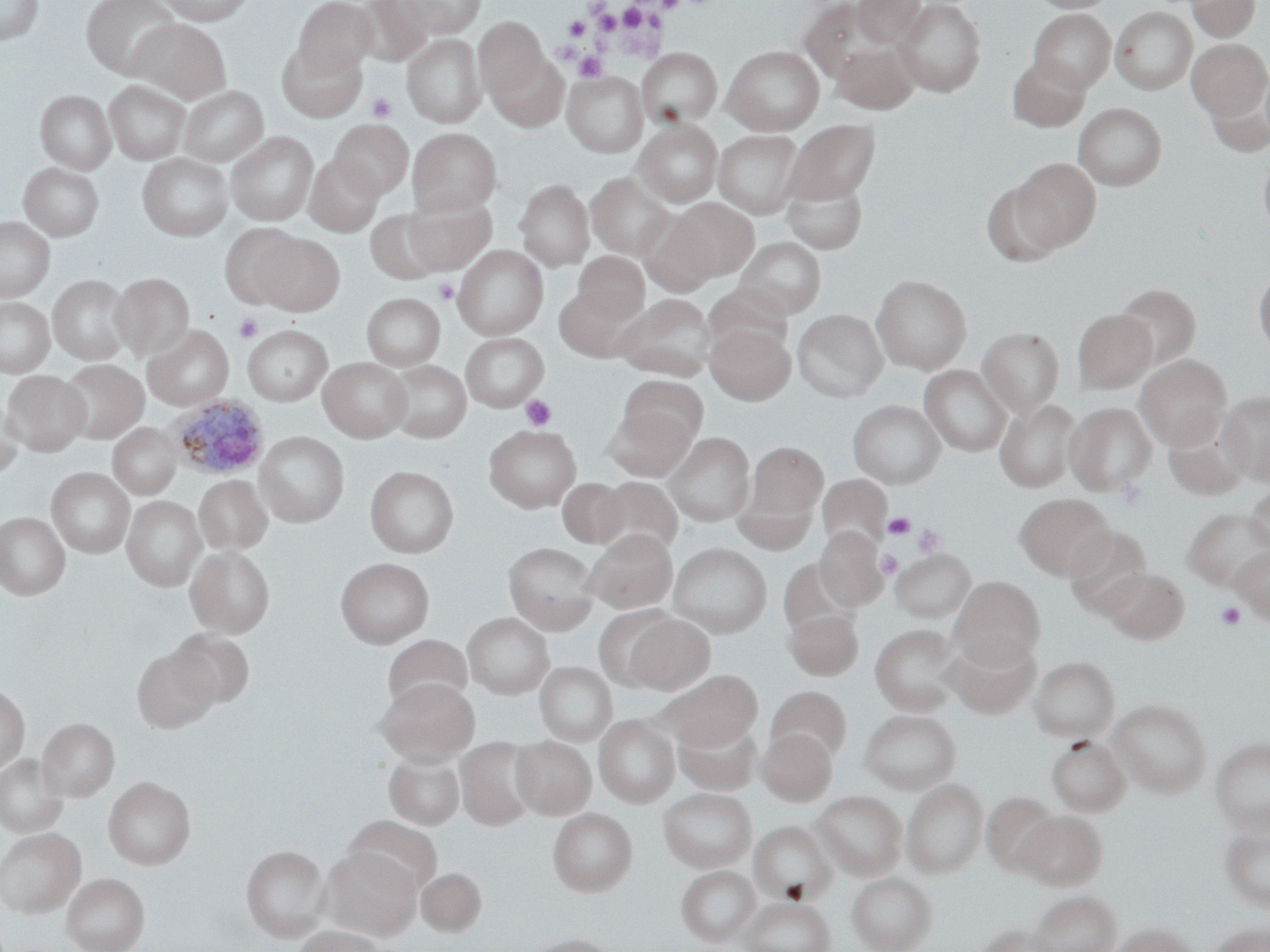
Summary:
  - Coordinate format: approximate bounding boxes as named x1/y1/x2/y2 corners in pixels
  - Platelet locations: (x1=618, y1=3, x2=650, y2=30), (x1=590, y1=5, x2=621, y2=33), (x1=565, y1=16, x2=590, y2=39), (x1=573, y1=51, x2=607, y2=82), (x1=367, y1=93, x2=397, y2=122), (x1=433, y1=278, x2=460, y2=304), (x1=234, y1=315, x2=262, y2=342), (x1=520, y1=394, x2=556, y2=430), (x1=883, y1=512, x2=915, y2=539), (x1=912, y1=523, x2=945, y2=557), (x1=876, y1=551, x2=903, y2=579), (x1=1215, y1=602, x2=1246, y2=631)
  - Uninfected red blood cell locations: (x1=0, y1=0, x2=43, y2=44), (x1=82, y1=0, x2=181, y2=79), (x1=160, y1=0, x2=253, y2=25), (x1=293, y1=0, x2=378, y2=76), (x1=354, y1=0, x2=433, y2=67), (x1=399, y1=0, x2=485, y2=37), (x1=852, y1=0, x2=928, y2=47), (x1=894, y1=0, x2=986, y2=96), (x1=1025, y1=0, x2=1119, y2=13), (x1=1186, y1=0, x2=1261, y2=41), (x1=799, y1=1, x2=891, y2=83), (x1=1111, y1=6, x2=1197, y2=94), (x1=1028, y1=9, x2=1116, y2=92), (x1=475, y1=17, x2=548, y2=99), (x1=127, y1=19, x2=231, y2=104), (x1=403, y1=34, x2=485, y2=127), (x1=1187, y1=39, x2=1270, y2=119), (x1=277, y1=41, x2=366, y2=121), (x1=831, y1=41, x2=918, y2=114), (x1=721, y1=45, x2=825, y2=135), (x1=636, y1=48, x2=722, y2=128), (x1=488, y1=52, x2=569, y2=133), (x1=1006, y1=56, x2=1091, y2=132), (x1=564, y1=72, x2=647, y2=157), (x1=104, y1=80, x2=190, y2=165), (x1=1205, y1=81, x2=1270, y2=157), (x1=178, y1=86, x2=268, y2=166), (x1=36, y1=90, x2=115, y2=174), (x1=1073, y1=103, x2=1168, y2=190), (x1=633, y1=118, x2=723, y2=208), (x1=330, y1=120, x2=414, y2=199), (x1=786, y1=120, x2=881, y2=203), (x1=408, y1=128, x2=501, y2=215), (x1=226, y1=130, x2=319, y2=226), (x1=714, y1=130, x2=802, y2=217), (x1=1258, y1=149, x2=1270, y2=240), (x1=137, y1=153, x2=232, y2=241), (x1=303, y1=154, x2=383, y2=237), (x1=1012, y1=158, x2=1101, y2=251), (x1=19, y1=163, x2=103, y2=241), (x1=781, y1=171, x2=868, y2=254), (x1=586, y1=172, x2=675, y2=260), (x1=514, y1=178, x2=594, y2=271), (x1=980, y1=179, x2=1066, y2=267), (x1=402, y1=196, x2=496, y2=274), (x1=671, y1=198, x2=759, y2=280), (x1=365, y1=210, x2=444, y2=284), (x1=638, y1=212, x2=717, y2=296), (x1=0, y1=217, x2=54, y2=301), (x1=218, y1=224, x2=302, y2=308), (x1=256, y1=233, x2=344, y2=316), (x1=734, y1=237, x2=826, y2=319), (x1=453, y1=245, x2=548, y2=339), (x1=574, y1=252, x2=649, y2=321), (x1=1254, y1=262, x2=1270, y2=360), (x1=110, y1=272, x2=193, y2=359), (x1=47, y1=274, x2=134, y2=365), (x1=871, y1=275, x2=971, y2=374), (x1=1114, y1=283, x2=1201, y2=368), (x1=703, y1=284, x2=792, y2=358), (x1=553, y1=287, x2=630, y2=361), (x1=361, y1=293, x2=445, y2=370), (x1=616, y1=294, x2=716, y2=379), (x1=0, y1=297, x2=54, y2=377), (x1=792, y1=308, x2=888, y2=402), (x1=1072, y1=309, x2=1157, y2=394), (x1=705, y1=323, x2=795, y2=404), (x1=143, y1=325, x2=234, y2=410), (x1=242, y1=325, x2=332, y2=404), (x1=977, y1=327, x2=1065, y2=417), (x1=460, y1=333, x2=548, y2=411), (x1=1135, y1=355, x2=1232, y2=448), (x1=318, y1=357, x2=411, y2=442), (x1=59, y1=359, x2=148, y2=443), (x1=383, y1=360, x2=471, y2=443), (x1=919, y1=365, x2=1013, y2=456), (x1=3, y1=371, x2=89, y2=455), (x1=619, y1=375, x2=708, y2=448), (x1=1218, y1=392, x2=1270, y2=485), (x1=0, y1=397, x2=23, y2=481), (x1=995, y1=398, x2=1082, y2=493), (x1=847, y1=400, x2=946, y2=488), (x1=1064, y1=402, x2=1157, y2=495), (x1=603, y1=408, x2=696, y2=481), (x1=1164, y1=414, x2=1249, y2=500), (x1=108, y1=423, x2=181, y2=498), (x1=483, y1=424, x2=582, y2=512), (x1=256, y1=432, x2=349, y2=526), (x1=664, y1=432, x2=755, y2=526), (x1=744, y1=441, x2=829, y2=524), (x1=365, y1=466, x2=459, y2=557), (x1=46, y1=468, x2=134, y2=558), (x1=194, y1=475, x2=272, y2=553), (x1=817, y1=475, x2=891, y2=552), (x1=595, y1=477, x2=683, y2=559), (x1=557, y1=478, x2=629, y2=548), (x1=1245, y1=483, x2=1270, y2=556), (x1=733, y1=485, x2=816, y2=555), (x1=1014, y1=493, x2=1115, y2=580), (x1=122, y1=496, x2=206, y2=591), (x1=1182, y1=507, x2=1270, y2=590), (x1=0, y1=512, x2=70, y2=600), (x1=814, y1=525, x2=888, y2=610), (x1=1063, y1=525, x2=1153, y2=615), (x1=584, y1=528, x2=677, y2=613), (x1=503, y1=542, x2=599, y2=634), (x1=668, y1=542, x2=772, y2=638), (x1=1230, y1=544, x2=1270, y2=625), (x1=185, y1=545, x2=274, y2=638), (x1=891, y1=549, x2=975, y2=622), (x1=335, y1=557, x2=434, y2=648), (x1=778, y1=557, x2=859, y2=635), (x1=1100, y1=567, x2=1189, y2=644), (x1=949, y1=576, x2=1045, y2=667), (x1=593, y1=605, x2=680, y2=690), (x1=784, y1=610, x2=863, y2=680), (x1=462, y1=612, x2=554, y2=699), (x1=625, y1=615, x2=715, y2=695), (x1=870, y1=624, x2=965, y2=716), (x1=167, y1=629, x2=254, y2=708), (x1=942, y1=632, x2=1041, y2=718), (x1=382, y1=634, x2=473, y2=710), (x1=132, y1=645, x2=219, y2=733), (x1=1029, y1=656, x2=1120, y2=742), (x1=535, y1=662, x2=617, y2=746), (x1=657, y1=670, x2=763, y2=751), (x1=376, y1=678, x2=479, y2=764), (x1=0, y1=683, x2=29, y2=774), (x1=766, y1=686, x2=852, y2=764), (x1=1108, y1=699, x2=1211, y2=798), (x1=859, y1=709, x2=961, y2=794), (x1=594, y1=715, x2=680, y2=808), (x1=674, y1=716, x2=762, y2=796), (x1=38, y1=718, x2=119, y2=800), (x1=757, y1=727, x2=836, y2=805), (x1=511, y1=736, x2=595, y2=818), (x1=1046, y1=736, x2=1131, y2=816), (x1=456, y1=737, x2=539, y2=830), (x1=1210, y1=737, x2=1270, y2=834), (x1=384, y1=749, x2=465, y2=829), (x1=0, y1=754, x2=68, y2=838), (x1=103, y1=777, x2=195, y2=870), (x1=902, y1=778, x2=988, y2=878), (x1=658, y1=787, x2=756, y2=873), (x1=812, y1=790, x2=907, y2=880), (x1=982, y1=792, x2=1062, y2=875), (x1=548, y1=807, x2=637, y2=896), (x1=1015, y1=810, x2=1106, y2=890), (x1=345, y1=815, x2=443, y2=896), (x1=1219, y1=819, x2=1270, y2=912), (x1=749, y1=820, x2=836, y2=904), (x1=0, y1=828, x2=86, y2=918), (x1=241, y1=844, x2=330, y2=942), (x1=320, y1=847, x2=421, y2=940), (x1=676, y1=865, x2=761, y2=945), (x1=416, y1=867, x2=486, y2=938), (x1=847, y1=871, x2=936, y2=952), (x1=62, y1=873, x2=150, y2=952), (x1=1029, y1=890, x2=1120, y2=952), (x1=740, y1=896, x2=835, y2=952), (x1=1206, y1=921, x2=1270, y2=952), (x1=1112, y1=922, x2=1201, y2=952), (x1=974, y1=923, x2=1057, y2=952), (x1=293, y1=925, x2=384, y2=952), (x1=524, y1=934, x2=621, y2=952)
  - Plasmodium ovale-infected red blood cell locations: (x1=165, y1=396, x2=269, y2=481)
  - Slide-level diagnosis: Plasmodium ovale
  - Preparation: thin blood film
  - Image size: 1270×952 pixels
  - Magnification: 1000x
  - Modality: optical microscopy
  - Stain: May-Grünwald-Giemsa
  - Field of view: one of a larger specimen